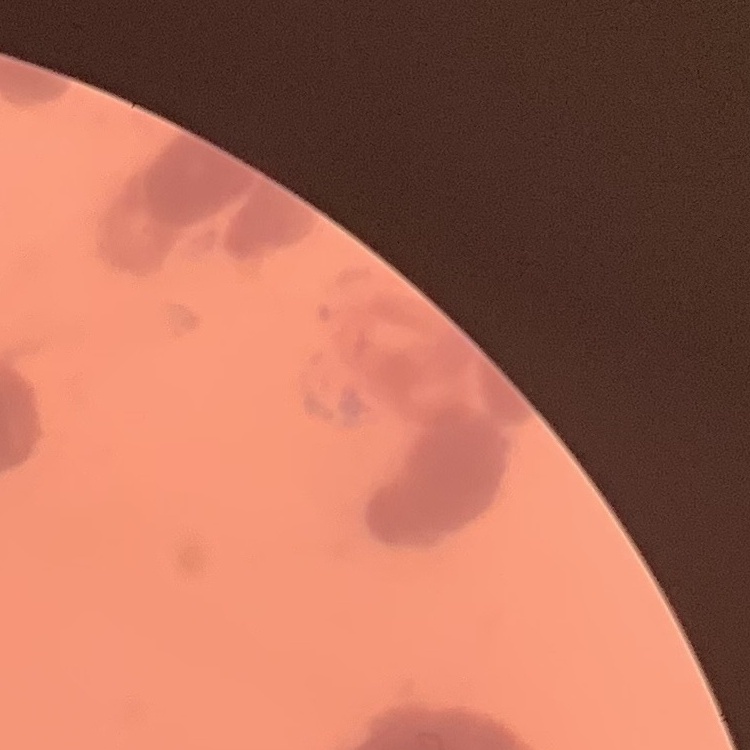

The erythrocytes show rouleaux formation. Field's or Giemsa stain. Thin blood smear. Square crop of a larger photomicrograph.